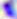
magnification = 400x
modality = micrograph
identification = Toxoplasma gondii